Report the malaria status of this cell.
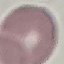
It is uninfected.

stain = Giemsa
capture = smartphone camera at the microscope eyepiece
image type = automatically extracted cell patch, resized to 64 × 64 pixels
preparation = thin smear